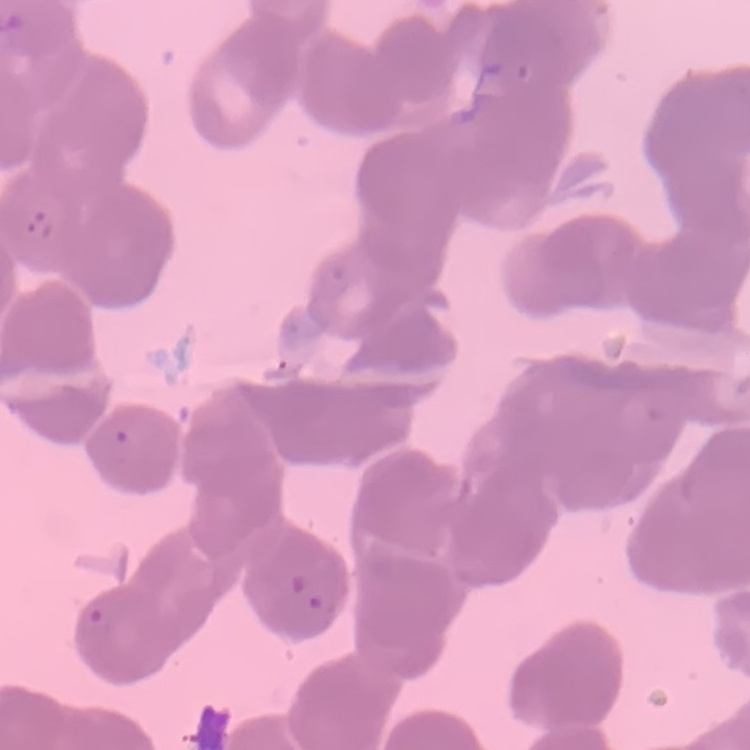
Summary:
  - Red blood cell morphology: rouleaux formation
  - Image type: square crop of a larger photomicrograph
  - Preparation: thin blood smear
  - Stain: Field's or Giemsa